Outline each uninfected red blood cell.
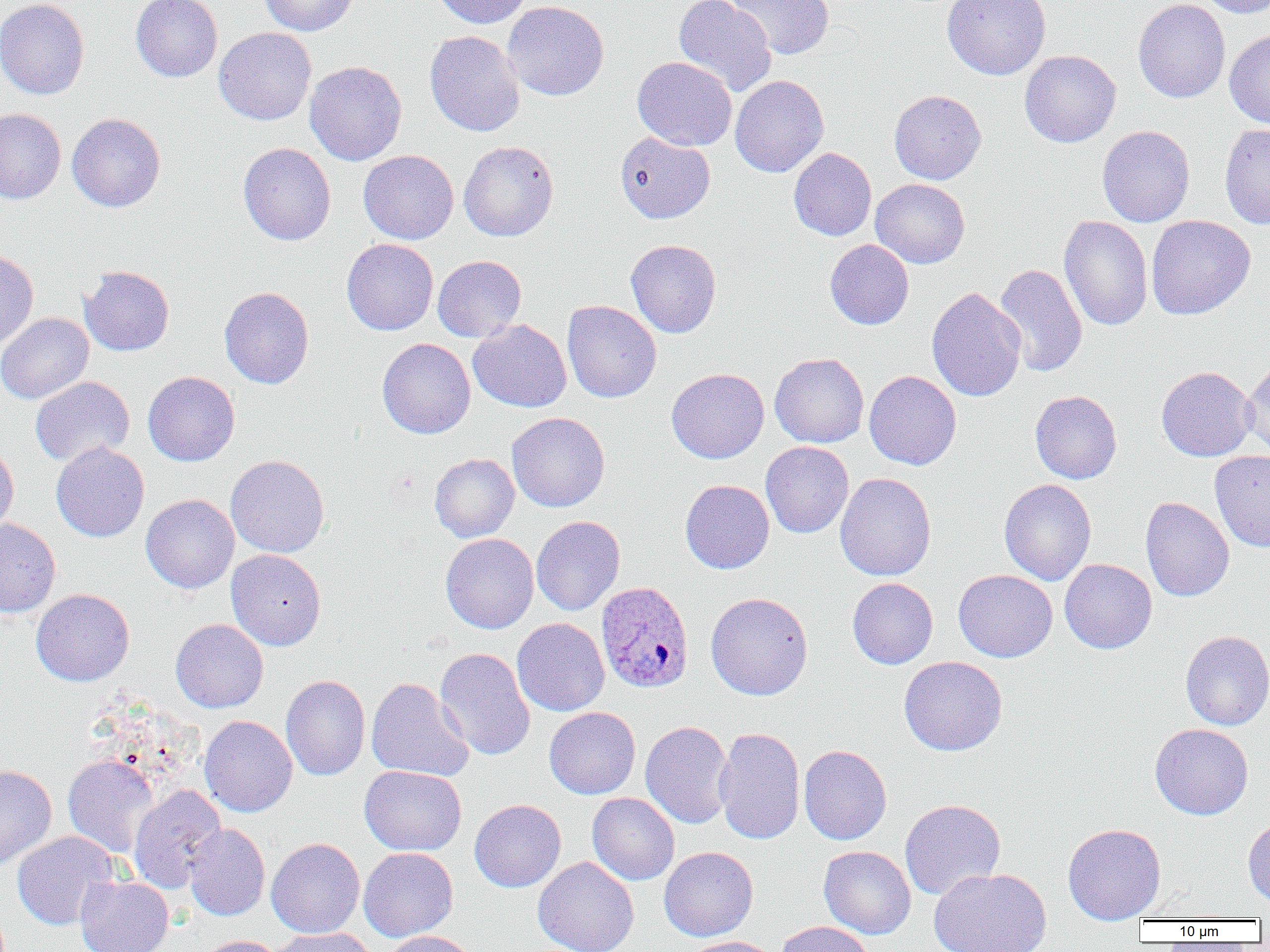
Approximate bounding boxes as (x1,y1)-(x2,y2) corner pairs in pixels.
Uninfected red blood cells: (0,0)-(90,100), (131,0)-(222,82), (259,0)-(358,36), (431,0)-(532,28), (673,0)-(777,96), (724,0)-(835,59), (942,0)-(1051,79), (1133,0)-(1230,103), (1196,0)-(1270,18), (502,1)-(609,101), (214,27)-(317,125), (1224,29)-(1270,128), (424,30)-(525,137), (1019,50)-(1121,147), (632,56)-(737,151), (305,61)-(407,166), (730,75)-(829,178), (889,90)-(986,184), (0,108)-(66,204), (67,113)-(166,212), (1219,122)-(1270,229), (1097,125)-(1195,227), (615,132)-(715,224), (458,140)-(559,241), (238,142)-(336,245), (788,147)-(876,241), (358,150)-(458,244), (870,178)-(970,268), (1058,215)-(1153,332), (1146,215)-(1255,320), (341,238)-(438,335), (625,239)-(722,338), (824,239)-(914,330), (0,249)-(39,351), (432,255)-(526,342), (582,259)-(689,365), (994,263)-(1088,377), (79,266)-(174,356), (219,286)-(314,389), (926,287)-(1026,402), (562,300)-(662,402), (0,312)-(94,404), (468,319)-(572,412), (377,337)-(476,439), (770,352)-(869,448), (1242,360)-(1270,458), (1156,366)-(1257,461), (666,368)-(769,463), (864,370)-(962,470), (143,371)-(240,466), (30,376)-(134,467), (1030,390)-(1122,484), (506,412)-(610,512), (51,441)-(149,542), (761,441)-(854,538), (0,444)-(19,539), (1210,449)-(1270,553), (429,453)-(519,542), (226,454)-(330,557), (835,472)-(936,581), (680,479)-(774,573), (999,479)-(1096,585), (140,494)-(239,594), (1140,496)-(1234,601), (531,515)-(625,615), (0,517)-(61,617), (440,533)-(539,633), (226,549)-(326,650), (1059,559)-(1157,654), (953,569)-(1057,662), (847,577)-(938,669), (30,588)-(134,686), (705,592)-(813,700), (512,618)-(609,716), (171,619)-(268,712), (1180,630)-(1270,730), (434,647)-(535,761), (899,655)-(1008,756), (281,674)-(370,781), (366,677)-(474,781), (544,707)-(641,799), (199,715)-(297,817), (640,720)-(734,829), (1149,723)-(1253,819), (714,726)-(805,845), (798,744)-(892,845), (62,754)-(160,858), (0,764)-(57,870), (360,765)-(467,855), (128,784)-(226,892), (587,793)-(680,885), (469,799)-(566,892), (899,799)-(1005,900), (1243,816)-(1270,907), (184,823)-(270,921), (1062,823)-(1166,924), (12,831)-(118,930), (266,838)-(365,938), (818,845)-(916,939), (659,846)-(758,941), (359,847)-(458,941), (533,857)-(639,952), (929,867)-(1052,952), (74,875)-(174,952), (776,921)-(874,952), (267,927)-(376,952), (382,930)-(478,952), (197,935)-(284,952), (683,936)-(779,952).

Plasmodium ovale-infected red blood cell locations: (596,581)-(694,693). Slide-level diagnosis: Plasmodium ovale. Thin blood smear. Single field of view. Captured at 1000x magnification. Image is 1270×952 pixels. Optical microscopy.